Assess this cell for malaria.
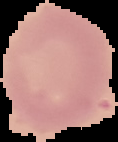

Uninfected.

From a thin blood smear. Image is 118×142 pixels. Cell region segmented out of the field of view; the surrounding area is masked to black.